Describe the morphology of the erythrocytes.
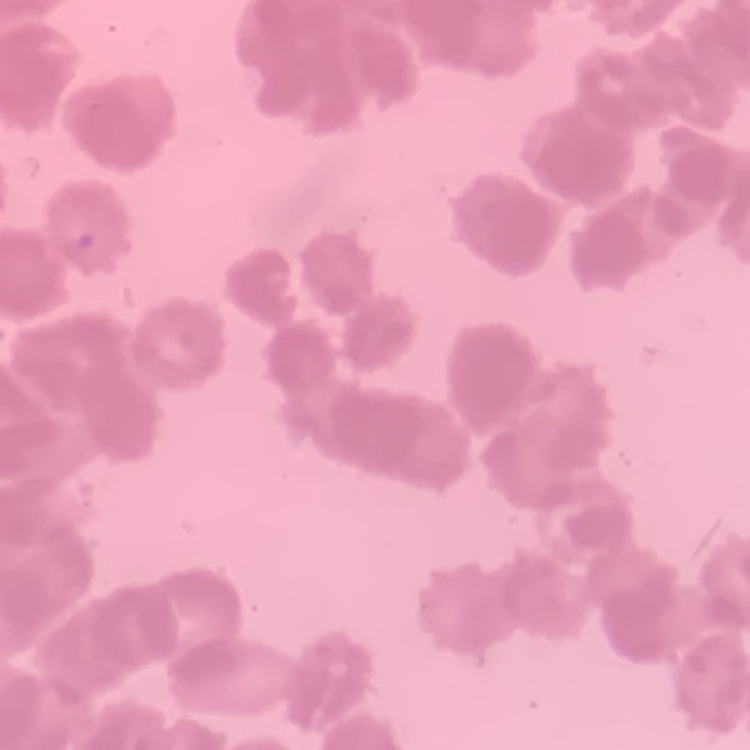

They show rouleaux formation.

image type = square crop of a larger photomicrograph
preparation = thin blood smear
stain = Field's or Giemsa